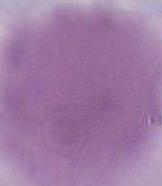
identification = erythrocyte
modality = micrograph
magnification = 1000x